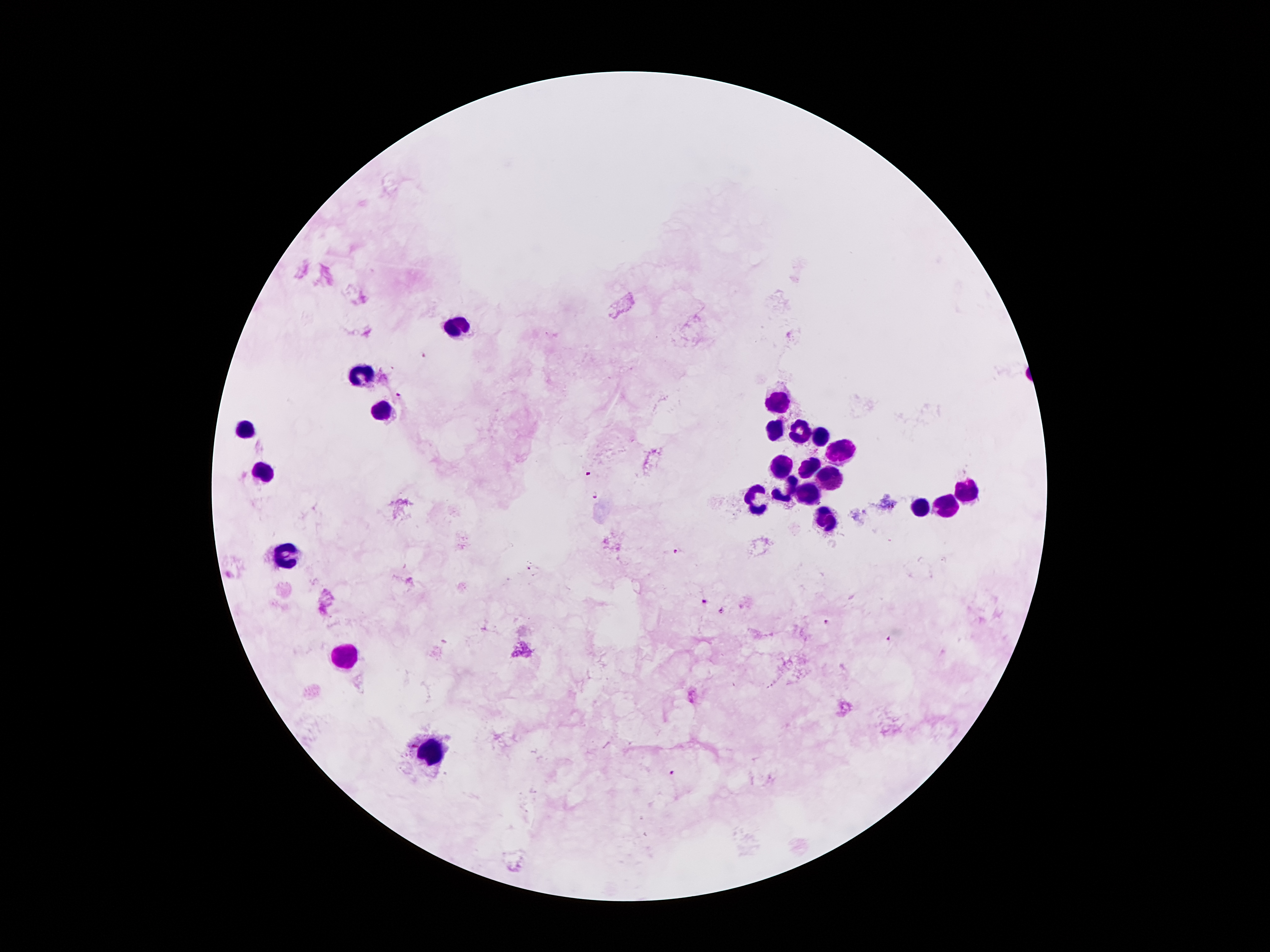
Approximate centers as {x, y} in pixels. Leukocyte locations: {454, 324}, {362, 375}, {778, 399}, {377, 411}, {773, 429}, {244, 431}, {795, 431}, {817, 436}, {842, 450}, {780, 460}, {807, 460}, {264, 468}, {830, 476}, {788, 485}, {966, 487}, {810, 492}, {760, 501}, {946, 503}, {921, 507}, {825, 518}, {283, 552}, {350, 655}, {432, 748}. Malaria parasite locations: {424, 356}, {398, 395}, {591, 474}, {595, 494}, {677, 552}, {703, 599}, {722, 612}, {827, 623}, {889, 637}, {672, 772}. Patient malaria status: infected with Plasmodium falciparum. Smartphone photograph taken through the microscope eyepiece. 100x magnification. Single field of view. Giemsa stain. Image is 1270×952 pixels. Thick peripheral-blood smear.